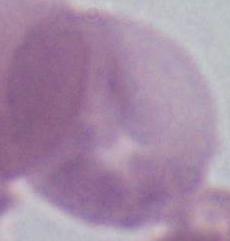
{
  "magnification": "1000x",
  "identification": "red blood cell",
  "modality": "micrograph"
}